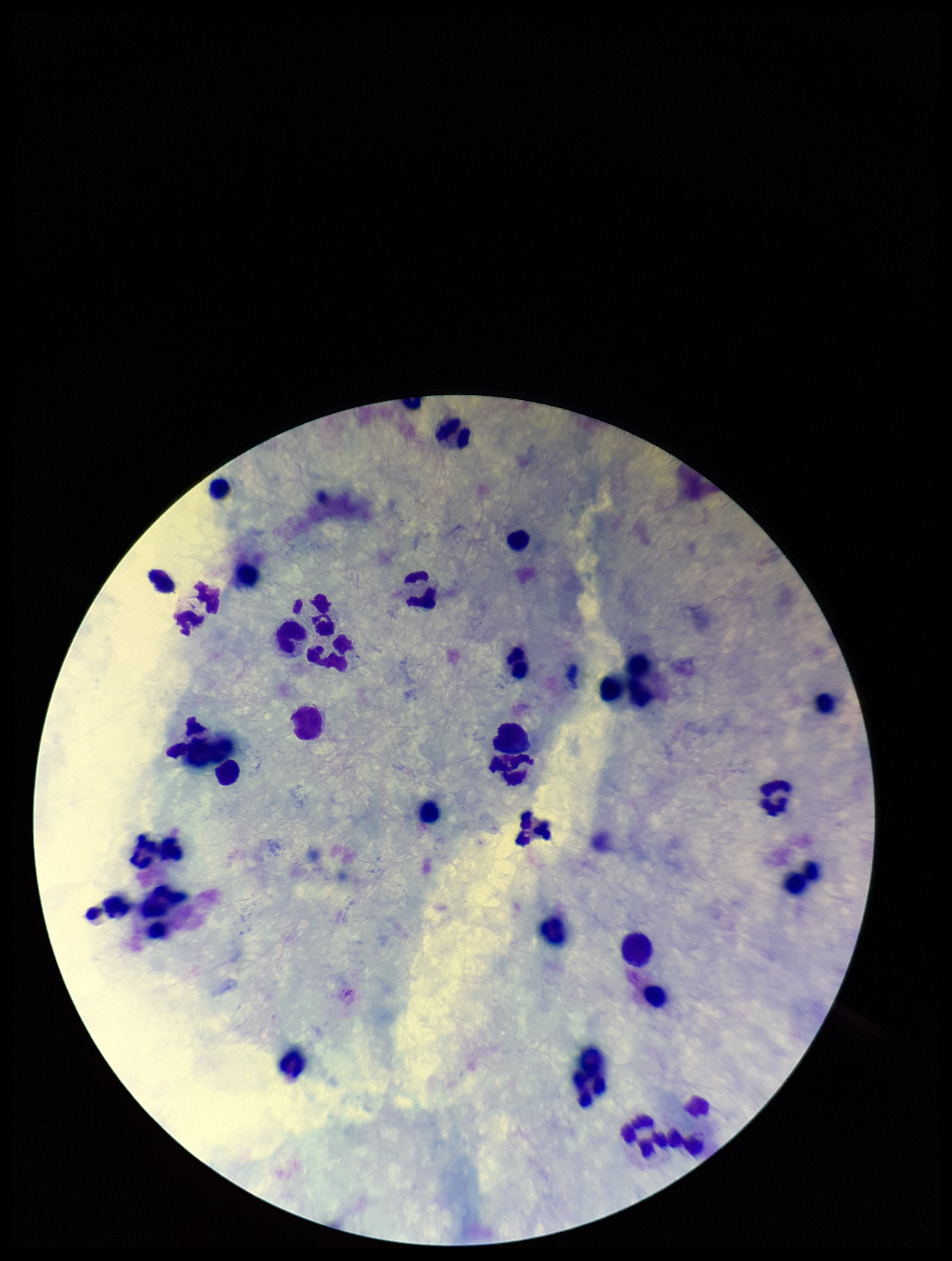
Stained with Giemsa. Smartphone photograph taken through the eyepiece of a microscope. One field from this slide. Image is 952×1261 pixels. Plasmodium parasites: none seen. Preparation: thick blood smear. Parasite count: 0. Leukocyte count: 34. Patient malaria status: negative.